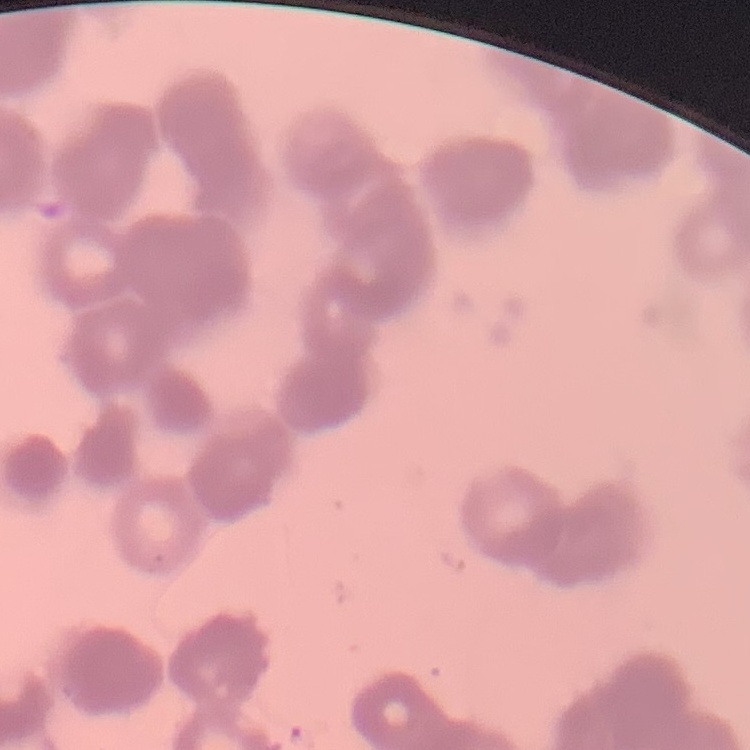

red blood cell morphology = rouleaux formation
image type = square crop of a larger photomicrograph
preparation = thin blood smear
stain = Field's or Giemsa